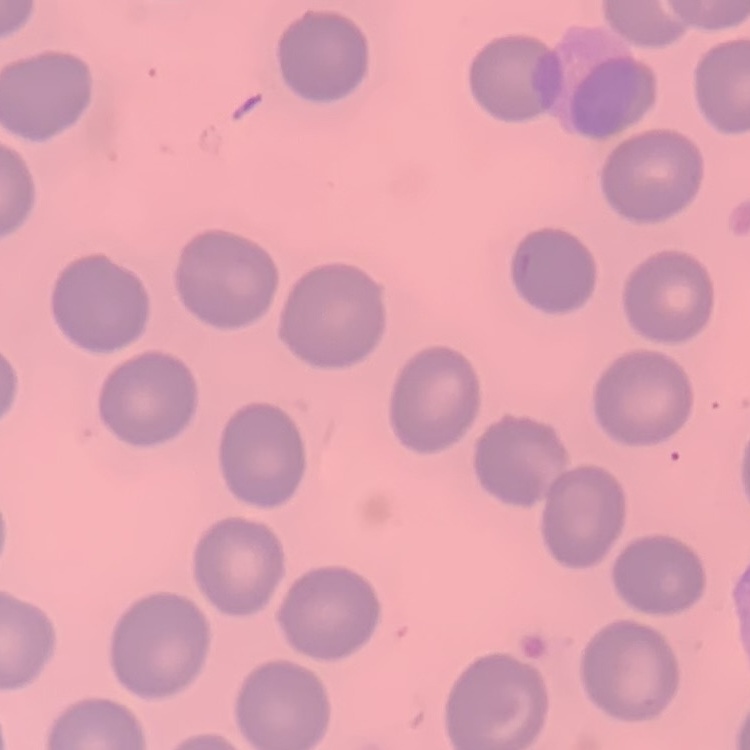

red blood cell morphology = no rouleaux formation
image type = square crop of a larger photomicrograph
stain = Field's or Giemsa
preparation = thin blood smear